Classify this cell by malaria status.
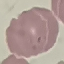
It is parasitized.

Automatically extracted cell patch, resized to 64 × 64 pixels. Giemsa-stained preparation. Acquired by smartphone through the microscope eyepiece. Thin blood film.